Classify this cell by malaria status.
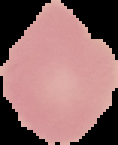

Uninfected.

image size = 118×145 pixels
image type = segmented cell region on a black background
preparation = thin blood film